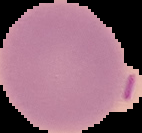

The area outside the segmented cell region is set to black. From a thin blood film. Image is 142×133 pixels. Malaria status: uninfected.